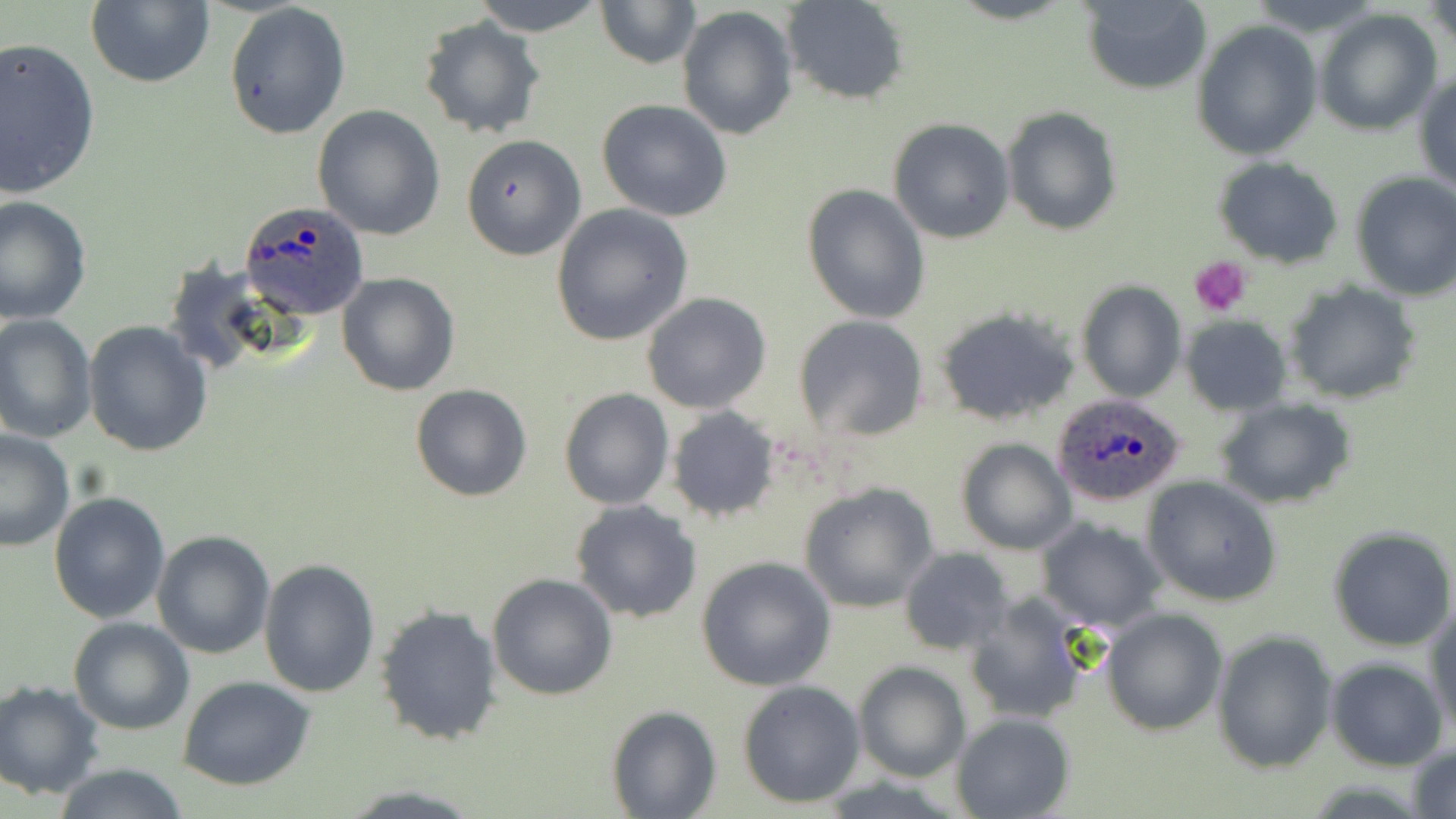

Summary:
  - Coordinate format: approximate bounding boxes as (x1, y1, x2, y2) in pixels
  - Platelet locations: (1190, 255, 1250, 317)
  - Plasmodium ovale-infected red blood cell locations: (238, 200, 371, 319), (1049, 392, 1187, 507)
  - Uninfected red blood cell locations: (85, 0, 216, 89), (468, 0, 607, 35), (595, 0, 700, 70), (781, 1, 911, 106), (1079, 1, 1212, 94), (223, 2, 351, 141), (1427, 2, 1454, 58), (677, 5, 799, 139), (1312, 8, 1442, 135), (416, 16, 548, 139), (1193, 20, 1322, 160), (0, 36, 101, 200), (1414, 69, 1456, 194), (597, 99, 733, 222), (312, 105, 445, 241), (1002, 107, 1122, 235), (888, 118, 1015, 244), (460, 135, 584, 260), (1213, 156, 1345, 268), (1349, 171, 1456, 302), (801, 183, 932, 324), (0, 194, 92, 324), (551, 203, 693, 345), (335, 271, 460, 396), (1078, 280, 1186, 402), (1285, 283, 1423, 404), (641, 291, 771, 414), (933, 306, 1081, 426), (0, 313, 97, 443), (794, 314, 930, 441), (1181, 316, 1291, 416), (82, 321, 213, 457), (409, 383, 532, 502), (558, 387, 674, 510), (1217, 398, 1355, 510), (666, 406, 781, 522), (0, 429, 77, 552), (954, 438, 1076, 554), (1142, 477, 1282, 607), (797, 482, 940, 614), (48, 491, 170, 624), (569, 500, 702, 623), (1034, 517, 1168, 633), (1329, 527, 1456, 650), (151, 530, 275, 659), (899, 546, 1015, 656), (694, 555, 837, 690), (259, 558, 381, 697), (487, 572, 619, 701), (963, 590, 1098, 725), (375, 604, 504, 746), (1426, 604, 1456, 737), (1100, 607, 1228, 734), (69, 616, 196, 735), (1212, 630, 1338, 774), (1325, 657, 1449, 770), (853, 661, 971, 782), (176, 675, 317, 790), (1, 679, 105, 799), (737, 680, 866, 808), (606, 704, 720, 818), (951, 712, 1076, 819), (1408, 741, 1456, 819), (52, 763, 192, 818)
  - Slide-level diagnosis: Plasmodium ovale
  - Stain: May-Grünwald-Giemsa
  - Field of view: single
  - Preparation: thin blood film
  - Image size: 1456×819 pixels
  - Magnification: 1000x
  - Modality: light microscopy